Assess this cell for malaria.
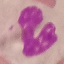

It is uninfected.

{
  "stain": "Giemsa",
  "preparation": "thin blood film",
  "capture": "smartphone camera at the microscope eyepiece",
  "image_type": "cell patch, automatically extracted from a larger field of view and resized to 64 × 64 pixels"
}